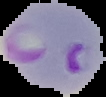

Summary:
  - Result: malaria parasites detected
  - Preparation: thin blood film
  - Image size: 106×97 pixels
  - Image type: segmented cell region on a black background